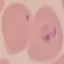
Malaria status: parasitized. Acquired by smartphone through the microscope eyepiece. Thin blood film. Giemsa-stained preparation. Automatically extracted cell patch, resized to 64 × 64 pixels.